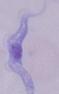

magnification: 1000x
identification: trypanosome
modality: photomicrograph